Comment on the morphology of the erythrocytes.
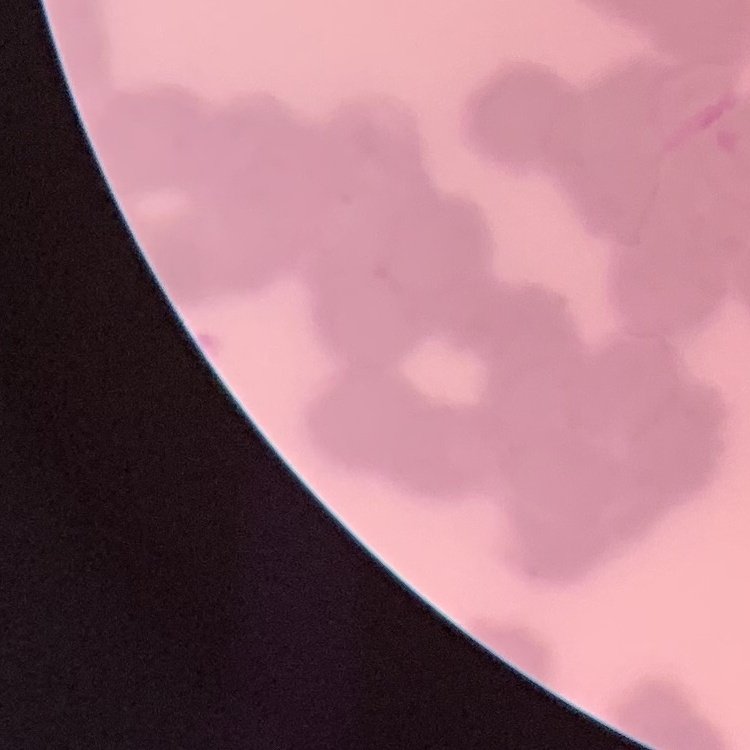
They show rouleaux formation.

Thin blood film. Field's or Giemsa stain. One tile cut from a larger photomicrograph.